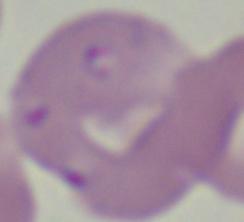

{
  "magnification": "1000x",
  "identification": "Babesia",
  "modality": "photomicrograph"
}